State which parasite is depicted.
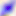

Toxoplasma gondii.

Micrograph. 400x magnification.